Report the malaria status of this cell.
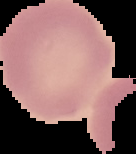

Uninfected.

preparation: thin blood film
image_size: 136×154 pixels
image_type: segmented cell region on a black background